Assess this cell for malaria.
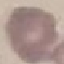
It is uninfected.

image type = automatically extracted cell patch, resized to 64 × 64 pixels
capture = smartphone camera at the microscope eyepiece
stain = Giemsa
preparation = thin blood smear